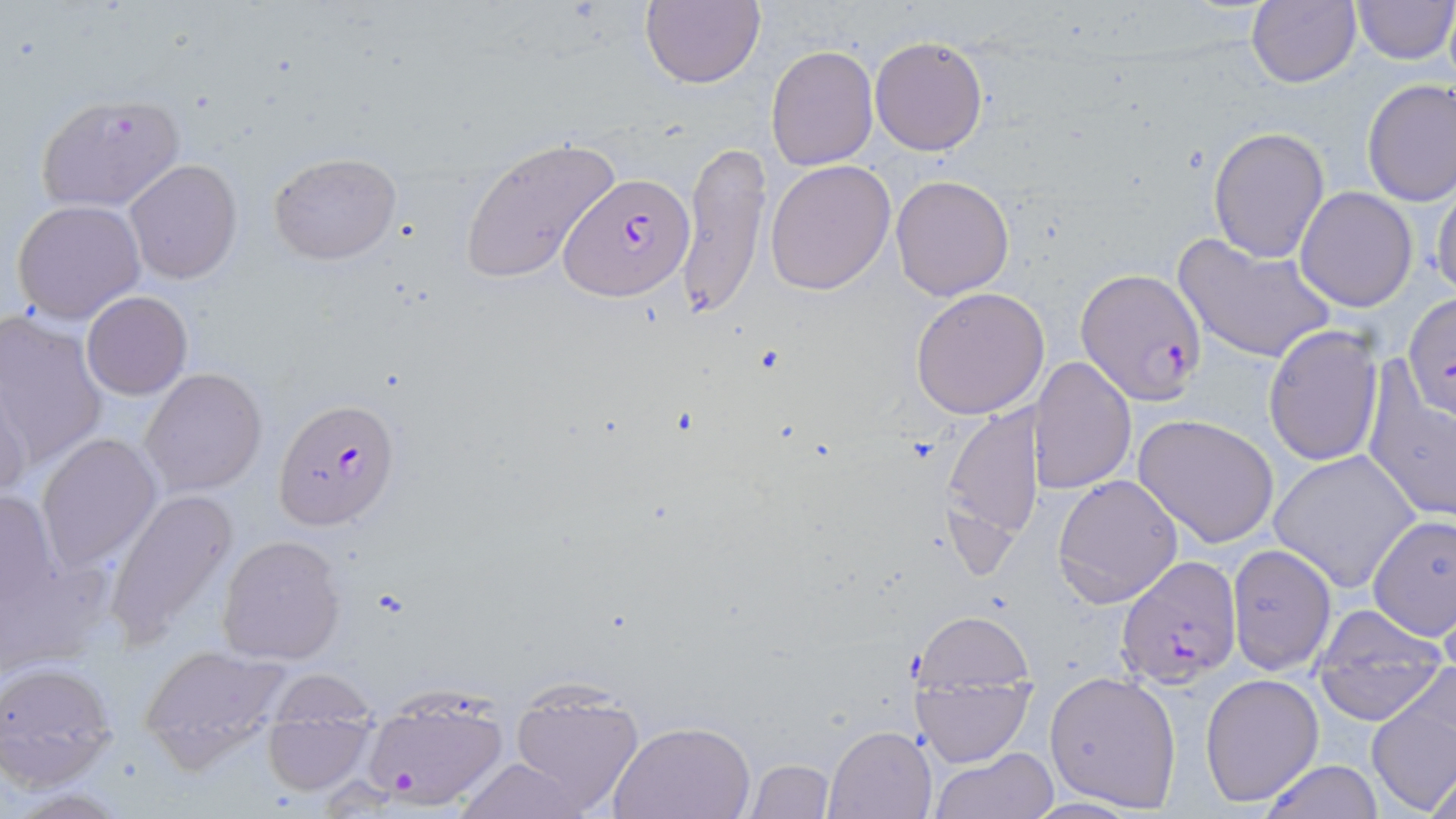
slide-level diagnosis = Plasmodium falciparum
uninfected red blood cell locations = approximate bounding boxes as (x1,y1)-(x2,y2) corner pairs in pixels: (640,0)-(765,89), (1246,0)-(1362,89), (1352,0)-(1453,64), (868,34)-(991,156), (766,45)-(879,171), (1361,78)-(1456,206), (34,92)-(186,213), (1208,127)-(1330,264), (458,135)-(622,286), (675,137)-(770,323), (268,152)-(403,264), (124,159)-(243,285), (765,160)-(896,296), (1429,173)-(1456,300), (889,174)-(1015,300), (1295,187)-(1418,312), (10,198)-(145,322), (1174,232)-(1338,364), (910,287)-(1050,420), (81,291)-(192,399), (0,316)-(108,471), (1261,324)-(1383,469), (1029,357)-(1137,493), (1363,360)-(1456,527), (140,367)-(268,496), (0,380)-(35,505), (940,404)-(1046,550), (1132,413)-(1281,548), (36,433)-(164,572), (1269,451)-(1423,593), (1052,474)-(1184,608), (1,489)-(62,635), (104,489)-(238,650), (1366,514)-(1456,640), (0,532)-(109,675), (216,534)-(347,666), (1226,544)-(1338,676), (1308,602)-(1450,725), (912,610)-(1035,703), (139,643)-(289,774), (907,649)-(1038,769), (0,659)-(117,790), (265,668)-(379,726), (1044,669)-(1183,811), (1201,673)-(1324,807), (1365,681)-(1455,817), (505,687)-(644,817), (361,690)-(510,811), (258,701)-(380,797), (608,719)-(757,819), (824,725)-(936,817), (932,747)-(1058,818), (452,756)-(594,819), (746,758)-(832,818), (1256,759)-(1386,818), (1425,763)-(1456,819)
modality = optical microscopy
preparation = thin blood smear
image size = 1456×819 pixels
Plasmodium falciparum-infected red blood cell locations = approximate bounding boxes as (x1,y1)-(x2,y2) corner pairs in pixels: (561,170)-(694,302), (1076,269)-(1208,403), (273,396)-(401,529), (1113,557)-(1242,688)
field of view = single
stain = May-Grünwald-Giemsa
magnification = 1000x